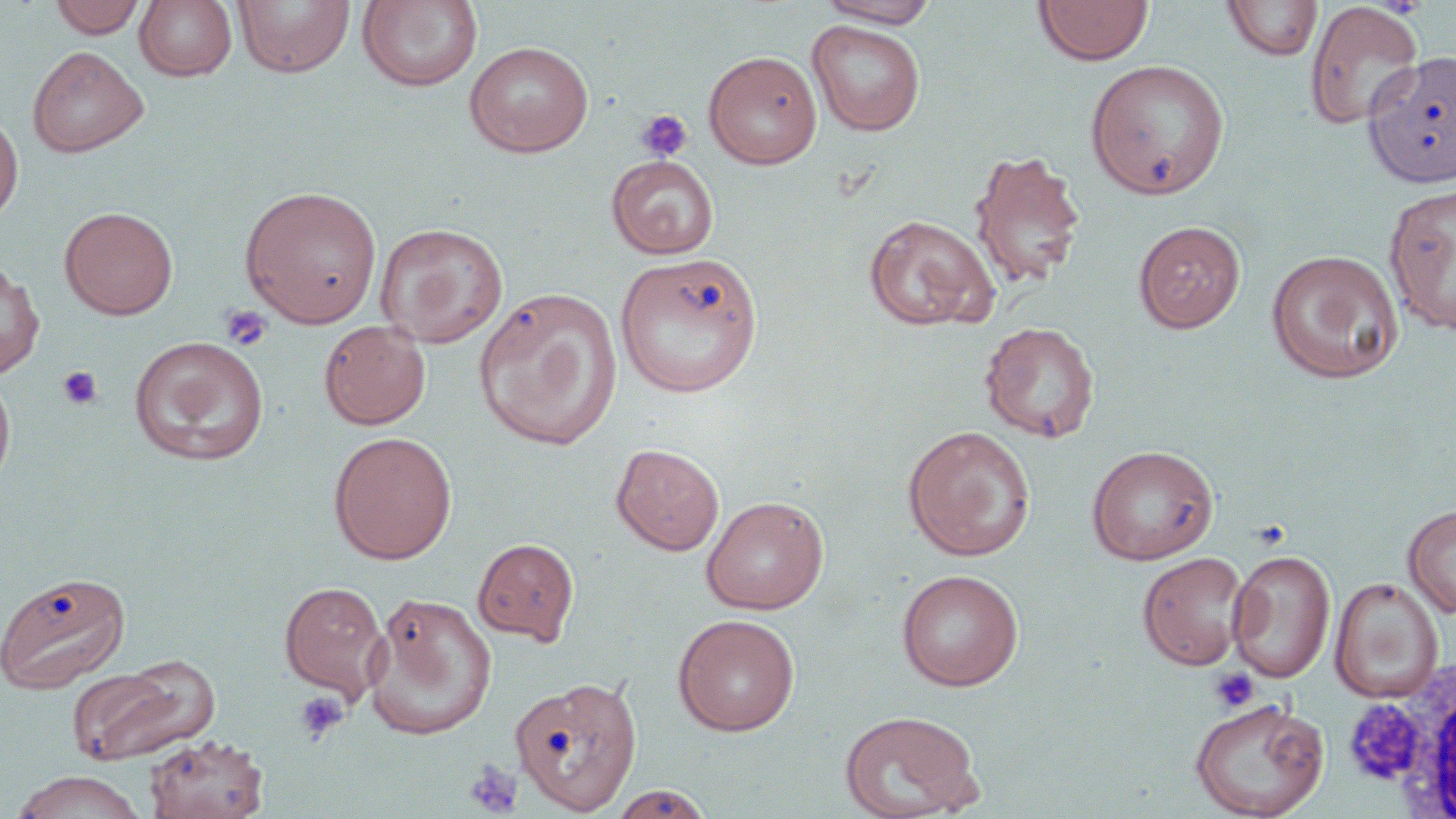

Summary:
  - Coordinate format: approximate bounding boxes as (x1, y1, x2, y2) in pixels
  - Platelet locations: (635, 109, 693, 161), (220, 305, 273, 351), (57, 365, 104, 409), (1209, 667, 1260, 714), (293, 690, 349, 744), (1339, 696, 1427, 787), (463, 760, 524, 818)
  - Uninfected red blood cell locations: (50, 0, 146, 38), (233, 0, 355, 79), (358, 0, 483, 93), (814, 0, 942, 27), (1033, 0, 1154, 66), (134, 1, 237, 82), (1222, 1, 1324, 62), (1304, 1, 1424, 132), (807, 19, 926, 136), (463, 41, 593, 157), (27, 45, 148, 158), (703, 50, 822, 168), (1363, 50, 1456, 189), (1084, 60, 1230, 200), (0, 111, 23, 224), (968, 149, 1087, 290), (606, 155, 719, 258), (1384, 183, 1456, 337), (239, 184, 382, 328), (60, 206, 178, 320), (863, 214, 1000, 332), (1133, 221, 1246, 333), (374, 223, 509, 348), (1265, 249, 1403, 384), (615, 252, 764, 398), (0, 262, 45, 378), (473, 287, 623, 450), (318, 319, 431, 430), (980, 321, 1100, 443), (129, 335, 270, 467), (0, 369, 16, 494), (902, 425, 1036, 561), (328, 431, 458, 565), (611, 443, 725, 556), (1086, 445, 1219, 564), (702, 495, 829, 615), (1403, 504, 1456, 618), (472, 538, 579, 645), (1227, 549, 1336, 683), (1137, 552, 1250, 670), (896, 569, 1024, 691), (0, 570, 131, 695), (1330, 577, 1444, 703), (279, 581, 390, 700), (363, 592, 498, 740), (673, 613, 800, 737), (67, 654, 219, 767), (510, 675, 643, 816), (1189, 697, 1329, 819), (838, 710, 983, 818), (143, 734, 269, 819), (9, 770, 148, 818), (608, 785, 716, 818)
  - White blood cell locations: (1396, 661, 1456, 813)
  - Slide-level diagnosis: no evidence of blood parasites
  - Preparation: thin blood smear
  - Magnification: 1000x
  - Modality: light microscopy
  - Stain: May-Grünwald-Giemsa
  - Field of view: one of a larger specimen
  - Image size: 1456×819 pixels